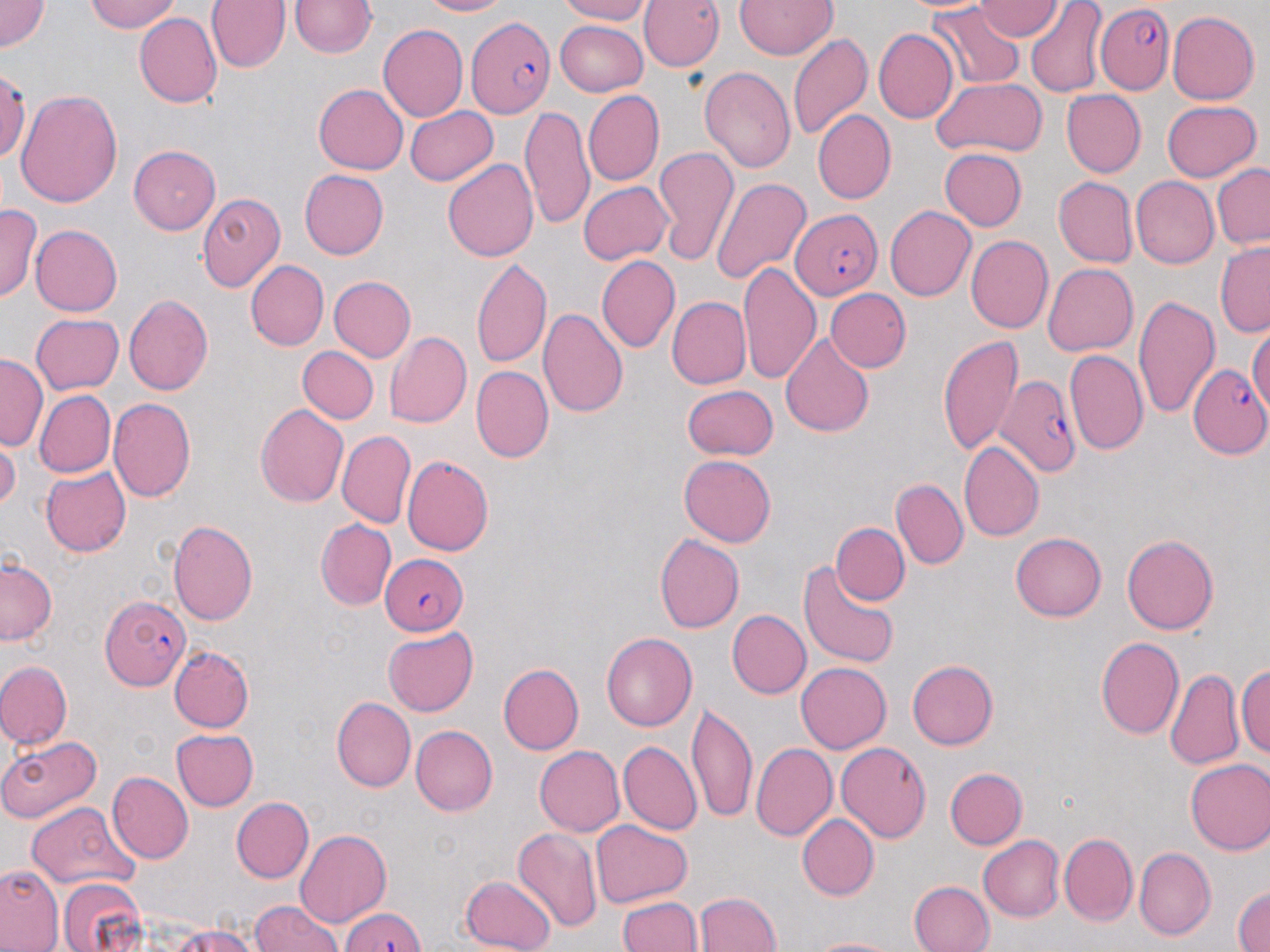

Approximate bounding boxes as (x1,y1)-(x2,y2) corner pairs in pixels. Uninfected red blood cell locations: (0,0)-(50,53), (85,0)-(183,34), (206,0)-(288,74), (288,0)-(379,60), (416,0)-(515,18), (552,0)-(652,24), (640,0)-(723,73), (975,0)-(1064,40), (735,1)-(837,61), (897,1)-(997,17), (1024,2)-(1105,97), (925,5)-(1028,87), (1167,11)-(1258,105), (137,12)-(222,109), (553,20)-(648,94), (376,24)-(466,123), (873,28)-(957,124), (787,34)-(872,141), (1,66)-(29,165), (701,66)-(795,174), (931,78)-(1047,158), (313,85)-(407,175), (14,89)-(122,208), (1059,89)-(1146,178), (583,91)-(664,185), (1161,100)-(1261,182), (406,105)-(499,186), (521,105)-(594,229), (811,111)-(894,204), (126,144)-(223,234), (653,146)-(737,267), (938,147)-(1029,231), (443,157)-(539,263), (1211,164)-(1270,250), (298,170)-(388,260), (709,175)-(812,286), (1131,175)-(1220,270), (1054,177)-(1137,267), (578,179)-(674,265), (199,191)-(285,293), (0,203)-(40,304), (884,205)-(975,301), (31,226)-(121,315), (965,235)-(1052,334), (1216,244)-(1269,337), (598,255)-(679,352), (471,259)-(550,368), (247,260)-(328,350), (738,261)-(820,386), (1041,264)-(1136,356), (329,276)-(415,362), (823,289)-(910,373), (122,294)-(212,398), (1132,294)-(1218,418), (665,297)-(750,389), (537,305)-(628,421), (30,313)-(124,394), (1246,324)-(1269,417), (386,330)-(471,427), (779,332)-(875,436), (937,334)-(1024,454), (298,347)-(379,426), (1064,349)-(1147,457), (0,355)-(44,449), (472,366)-(553,462), (682,384)-(780,460), (34,390)-(114,479), (107,398)-(197,504), (255,403)-(349,507), (336,430)-(414,527), (1,437)-(19,516), (960,443)-(1043,539), (402,455)-(493,555), (678,455)-(776,547), (42,466)-(131,555), (890,479)-(967,568), (168,519)-(258,624), (314,520)-(396,611), (830,522)-(907,607), (654,531)-(746,633), (1011,533)-(1106,622), (1121,534)-(1218,635), (1,557)-(57,648), (801,557)-(899,668), (726,610)-(810,699), (384,629)-(478,715), (600,631)-(697,730), (1094,636)-(1184,740), (171,644)-(254,731), (906,658)-(997,751), (1237,658)-(1270,763), (795,661)-(890,754), (0,662)-(71,750), (500,664)-(585,754), (1164,669)-(1245,771), (332,695)-(414,792), (685,702)-(756,822), (409,724)-(497,816), (170,728)-(257,810), (0,732)-(101,823), (617,742)-(701,837), (752,742)-(837,842), (836,742)-(930,843), (533,745)-(624,837), (1185,758)-(1270,856), (946,767)-(1027,850), (106,773)-(192,865), (231,797)-(313,882), (26,802)-(136,893), (795,813)-(876,900), (592,821)-(691,907), (514,828)-(601,935), (294,829)-(390,926), (978,834)-(1066,920), (1061,835)-(1137,925), (1133,847)-(1217,942), (2,867)-(61,952), (458,874)-(556,952), (55,877)-(149,952), (909,879)-(995,952), (1233,883)-(1269,952), (693,890)-(783,952), (616,894)-(701,952), (249,897)-(343,952), (167,926)-(260,952), (802,934)-(907,951). Plasmodium falciparum-infected red blood cell locations: (1096,5)-(1178,93), (465,16)-(553,119), (790,208)-(883,300), (1186,362)-(1270,458), (996,376)-(1079,474), (378,552)-(466,632), (99,592)-(193,689), (340,903)-(427,952). Slide-level diagnosis: Plasmodium falciparum. One field of a larger specimen. May-Grünwald-Giemsa stain. Thin blood smear. 1000x magnification. Image is 1270×952 pixels. Optical microscopy.